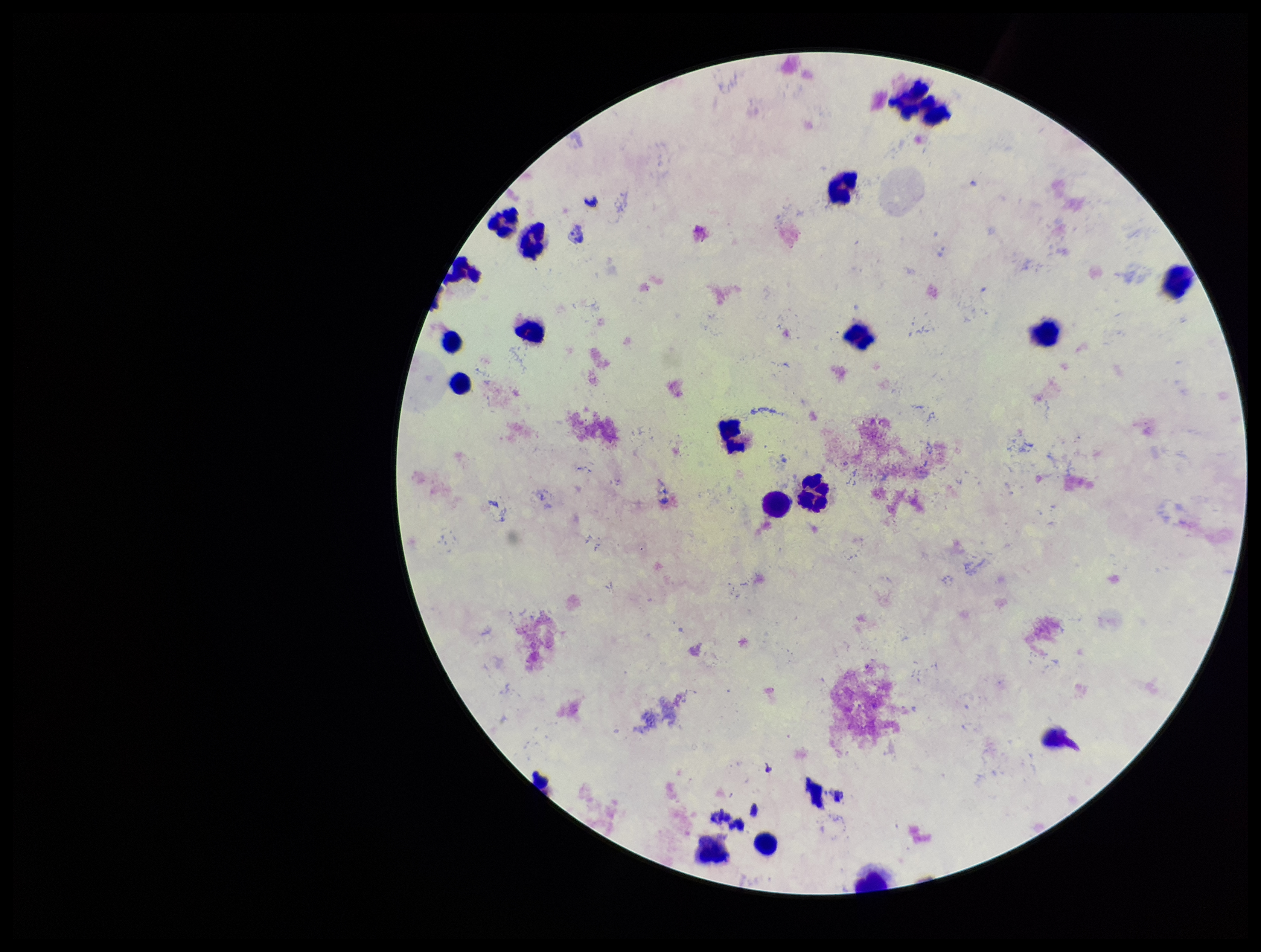
{
  "plasmodium_parasites": "none detected",
  "field_of_view": "one from this slide",
  "stain": "Giemsa",
  "patient_malaria_status": "positive",
  "preparation": "thick blood smear",
  "species_reported_for_this_patient": "Plasmodium vivax",
  "parasite_count": 0,
  "leukocyte_count": 18,
  "capture": "smartphone photograph through the microscope eyepiece",
  "image_size": "1261×952 pixels"
}